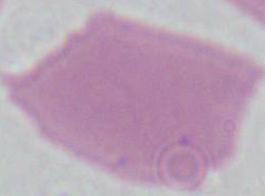

Summary:
  - Magnification: 1000x
  - Modality: micrograph
  - Identification: erythrocyte